Assess this cell for malaria.
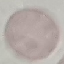
It is uninfected.

Summary:
  - Capture: smartphone camera at the microscope eyepiece
  - Image type: automatically extracted cell patch, resized to 64 × 64 pixels
  - Stain: Giemsa
  - Preparation: thin smear